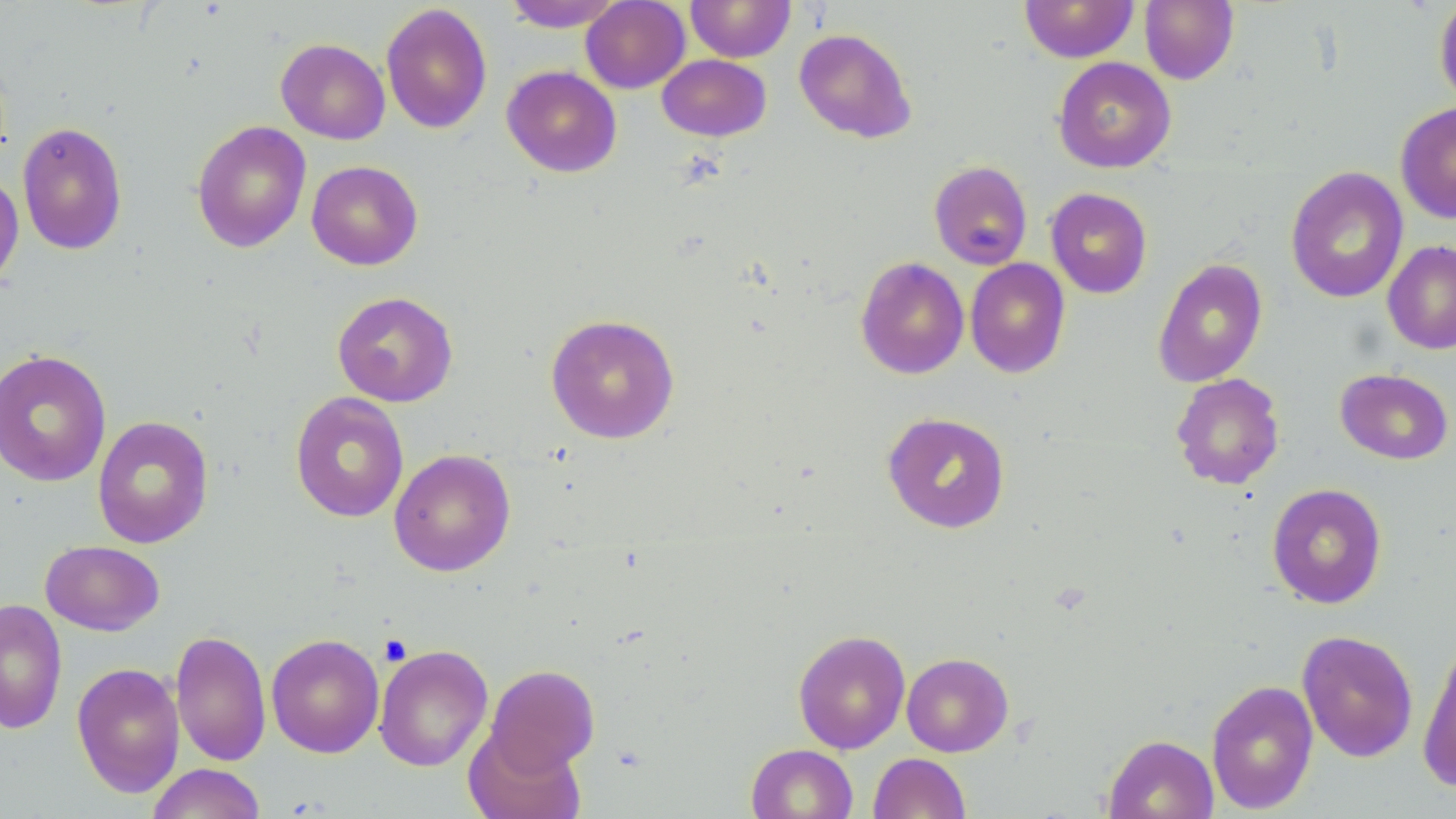
slide-level diagnosis = negative for blood parasites
magnification = 1000x
platelet locations = approximate bounding boxes as named x1/y1/x2/y2 corners in pixels: (x1=379, y1=635, x2=412, y2=665)
image size = 1456×819 pixels
modality = optical microscopy
preparation = thin blood film
uninfected red blood cell locations = approximate bounding boxes as named x1/y1/x2/y2 corners in pixels: (x1=503, y1=0, x2=625, y2=32), (x1=581, y1=0, x2=690, y2=93), (x1=687, y1=0, x2=795, y2=62), (x1=1019, y1=0, x2=1139, y2=63), (x1=1139, y1=0, x2=1239, y2=85), (x1=1434, y1=0, x2=1456, y2=108), (x1=380, y1=3, x2=493, y2=134), (x1=793, y1=28, x2=917, y2=143), (x1=276, y1=38, x2=390, y2=144), (x1=657, y1=54, x2=771, y2=141), (x1=1053, y1=56, x2=1176, y2=173), (x1=501, y1=65, x2=622, y2=177), (x1=1395, y1=101, x2=1456, y2=224), (x1=191, y1=120, x2=311, y2=253), (x1=16, y1=121, x2=128, y2=255), (x1=307, y1=160, x2=423, y2=270), (x1=929, y1=160, x2=1032, y2=270), (x1=1285, y1=166, x2=1409, y2=303), (x1=0, y1=171, x2=24, y2=291), (x1=1045, y1=187, x2=1152, y2=298), (x1=1382, y1=240, x2=1456, y2=354), (x1=855, y1=256, x2=969, y2=379), (x1=1152, y1=257, x2=1268, y2=388), (x1=965, y1=258, x2=1071, y2=378), (x1=332, y1=291, x2=458, y2=407), (x1=545, y1=314, x2=680, y2=444), (x1=0, y1=349, x2=112, y2=487), (x1=1335, y1=368, x2=1454, y2=465), (x1=1171, y1=373, x2=1285, y2=490), (x1=290, y1=392, x2=409, y2=522), (x1=882, y1=411, x2=1011, y2=533), (x1=92, y1=415, x2=214, y2=549), (x1=389, y1=449, x2=515, y2=576), (x1=1266, y1=483, x2=1387, y2=609), (x1=40, y1=540, x2=164, y2=636), (x1=0, y1=598, x2=68, y2=735), (x1=793, y1=629, x2=910, y2=754), (x1=171, y1=630, x2=272, y2=767), (x1=1297, y1=630, x2=1418, y2=762), (x1=266, y1=633, x2=384, y2=757), (x1=1417, y1=639, x2=1456, y2=792), (x1=374, y1=644, x2=493, y2=771), (x1=901, y1=652, x2=1014, y2=757), (x1=72, y1=662, x2=185, y2=798), (x1=486, y1=664, x2=600, y2=774), (x1=1206, y1=679, x2=1319, y2=814), (x1=463, y1=727, x2=585, y2=819), (x1=1103, y1=734, x2=1219, y2=819), (x1=746, y1=744, x2=858, y2=818), (x1=869, y1=752, x2=971, y2=818), (x1=145, y1=763, x2=267, y2=819)
stain = May-Grünwald-Giemsa
field of view = single